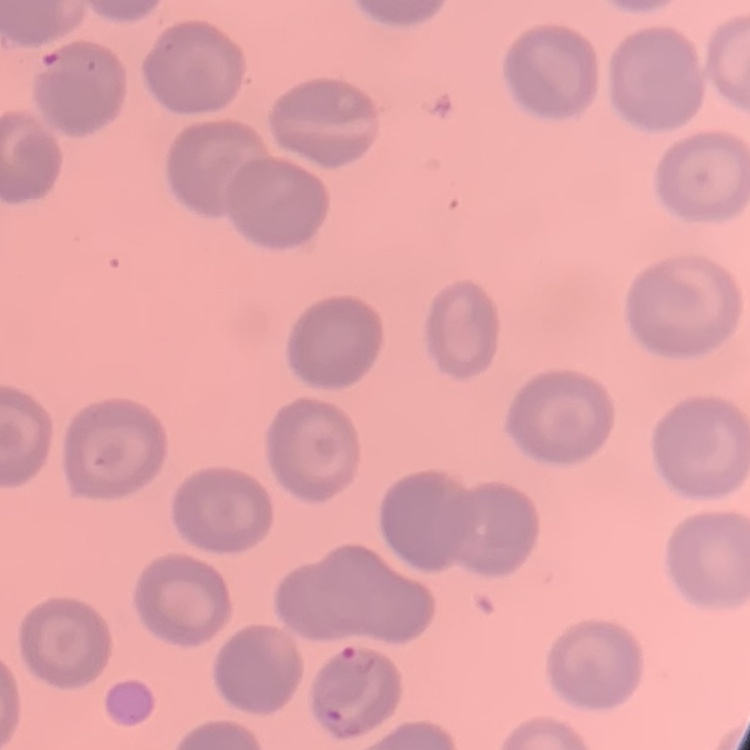
red blood cell morphology = no rouleaux formation
stain = Field's or Giemsa
preparation = thin blood film
image type = square crop of a larger photomicrograph